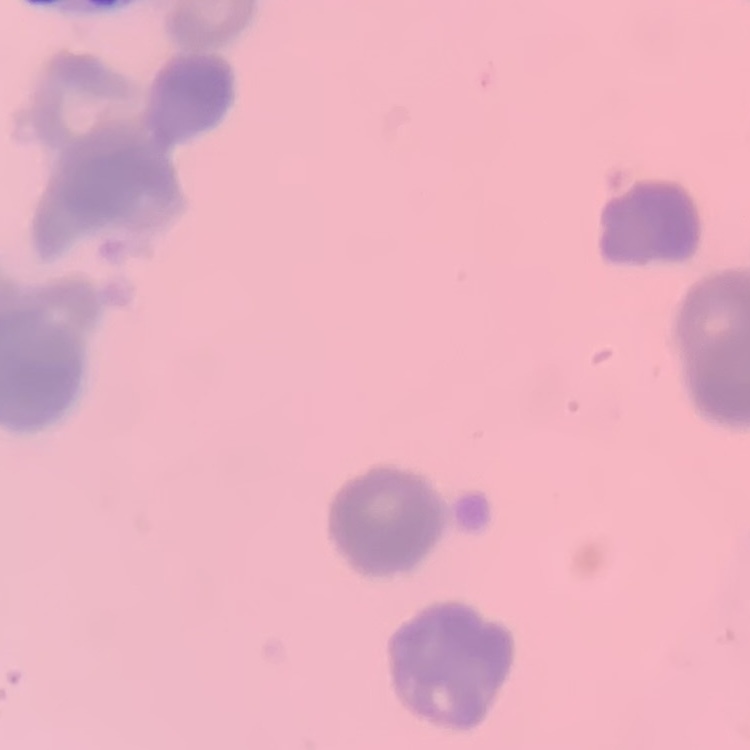
Summary:
  - Red blood cell morphology: rouleaux formation
  - Image type: square crop of a larger photomicrograph
  - Stain: Field's or Giemsa
  - Preparation: thin blood smear